Identify the blood parasite species.
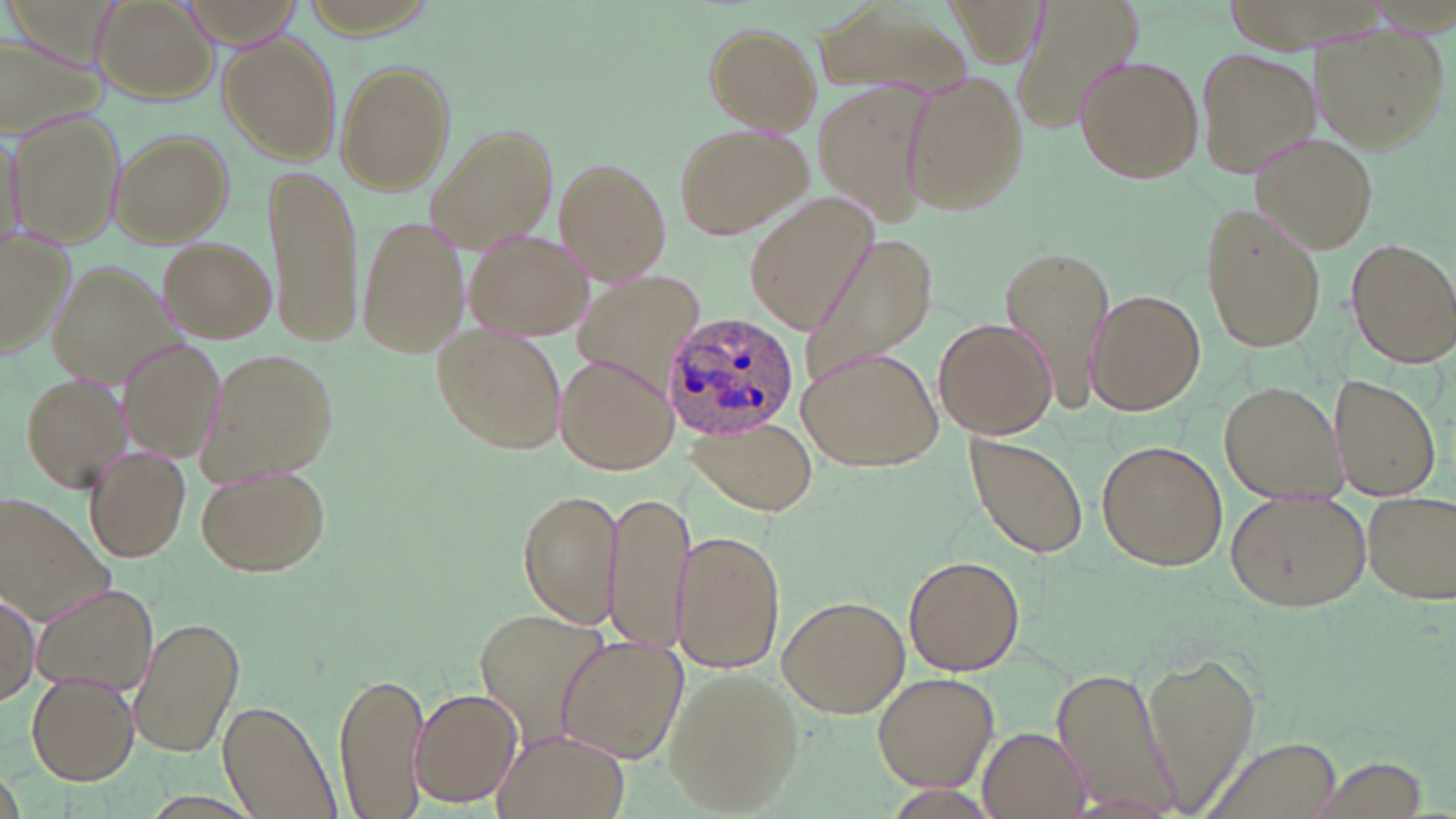

Plasmodium ovale.

Approximate bounding boxes as [x1, y1, x2, y2] in pixels. Plasmodium ovale-infected red blood cell locations: [664, 315, 802, 442]. Uninfected red blood cell locations: [91, 0, 217, 103], [1013, 0, 1143, 136], [809, 1, 972, 104], [702, 22, 823, 134], [1311, 25, 1448, 149], [0, 28, 109, 140], [220, 31, 342, 165], [1196, 46, 1319, 178], [1075, 55, 1204, 183], [334, 60, 456, 195], [901, 70, 1029, 215], [812, 76, 937, 230], [10, 111, 123, 249], [673, 122, 809, 242], [427, 125, 556, 252], [110, 129, 235, 246], [0, 132, 28, 257], [1253, 135, 1382, 254], [553, 157, 672, 285], [262, 162, 362, 344], [747, 194, 879, 330], [1202, 202, 1326, 353], [356, 214, 469, 361], [464, 228, 594, 340], [0, 232, 76, 360], [158, 237, 275, 343], [798, 237, 939, 388], [1345, 238, 1456, 365], [1000, 242, 1117, 412], [47, 260, 187, 387], [1087, 289, 1206, 416], [965, 294, 1099, 425], [932, 317, 1057, 439], [434, 325, 564, 455], [122, 341, 225, 458], [796, 346, 942, 470], [198, 347, 338, 483], [555, 353, 675, 475], [19, 372, 131, 492], [1334, 376, 1443, 500], [1221, 380, 1348, 504], [688, 419, 818, 511], [961, 433, 1088, 560], [1097, 440, 1226, 571], [84, 446, 190, 565], [197, 462, 331, 576], [517, 489, 622, 626], [1227, 489, 1371, 611], [602, 490, 692, 655], [1362, 491, 1455, 604], [0, 495, 115, 622], [671, 528, 784, 674], [903, 556, 1026, 678], [32, 585, 160, 698], [0, 592, 40, 704], [778, 594, 908, 717], [470, 606, 611, 753], [128, 616, 245, 762], [555, 636, 687, 763], [1141, 652, 1261, 808], [1049, 665, 1180, 811], [664, 669, 805, 814], [872, 670, 999, 792], [335, 672, 427, 818], [26, 673, 138, 784], [410, 688, 522, 808], [219, 699, 341, 818], [978, 729, 1088, 817], [490, 732, 629, 819], [1200, 734, 1344, 819]. 1000x magnification. Image is 1456×819 pixels. Light microscopy. Thin blood smear. May-Grünwald-Giemsa stain. One field of a larger specimen.